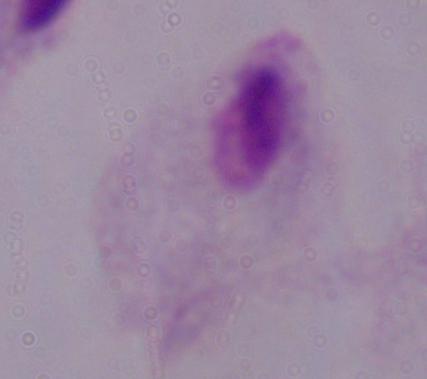

Summary:
  - Identification: trichomonad
  - Modality: photomicrograph
  - Magnification: 1000x